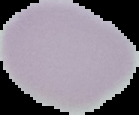

preparation: thin blood film
image_type: segmented cell region on a black background
image_size: 139×115 pixels
malaria_status: uninfected